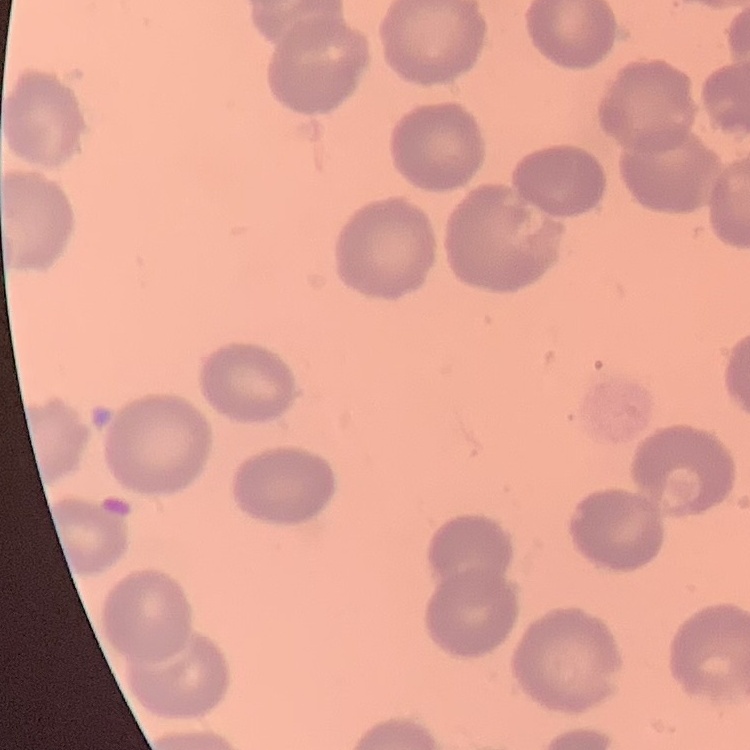 The red blood cells exhibit no rouleaux formation. Square crop of a larger photomicrograph. Thin peripheral smear. Field's or Giemsa stain.